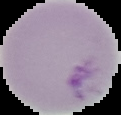

Summary:
  - Image type: segmented cell region on a black background
  - Malaria status: uninfected
  - Image size: 121×115 pixels
  - Preparation: thin blood film